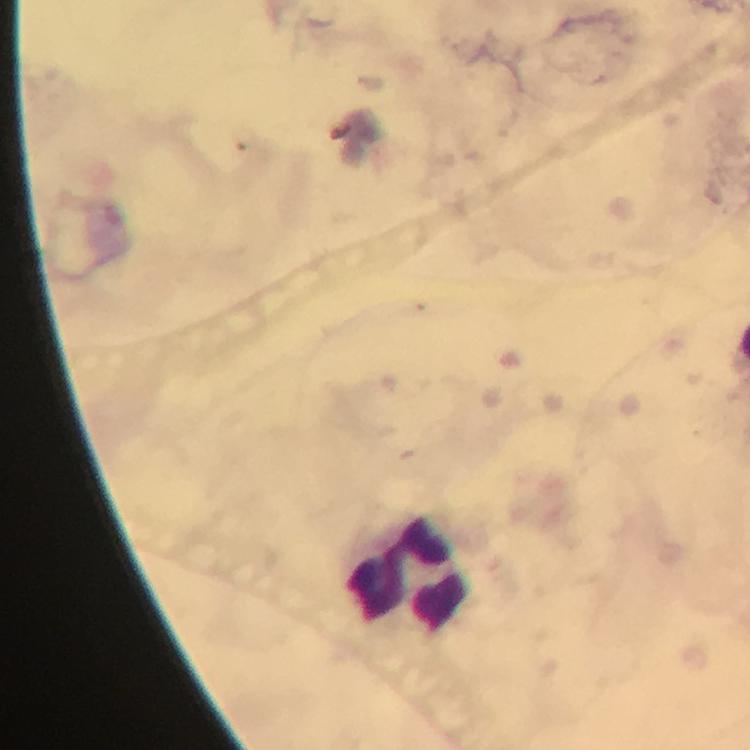

Approximate centers as {x, y} in pixels.
Summary:
  - Leukocyte locations: {412, 577}
  - Immersion oil: used
  - Context: from a malaria diagnostic workup
  - Plasmodium parasites: none seen
  - Stain: Giemsa
  - Preparation: thick blood smear
  - Cropped from: one field of view
  - Image size: 750×750 pixels
  - Capture: smartphone photograph through a microscope
  - Magnification: 100x